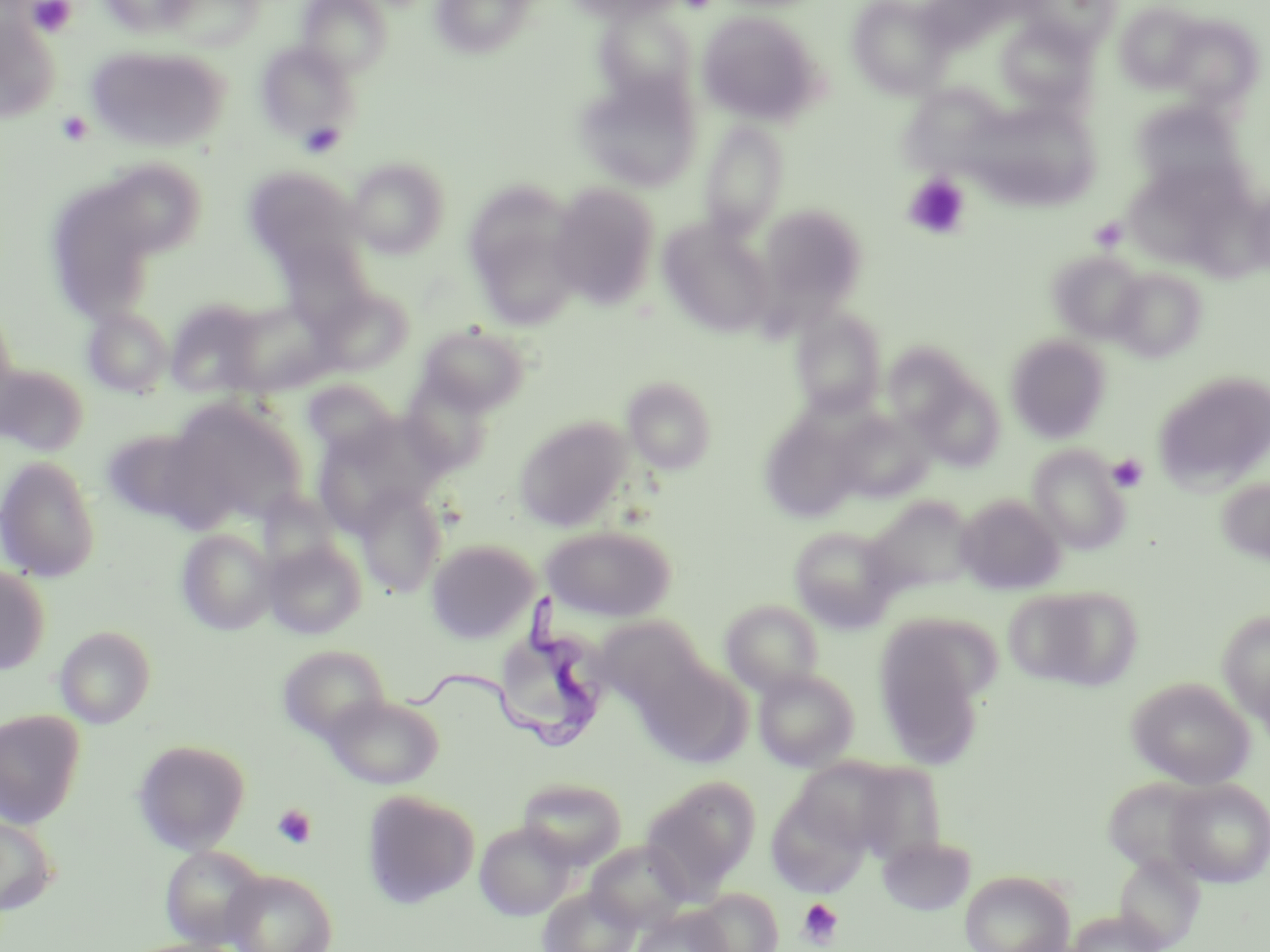
{
  "slide_level_diagnosis": "Trypanosoma brucei",
  "platelet_locations": "approximate bounding boxes as (x1,y1)-(x2,y2) corner pairs in pixels: (26,0)-(78,38), (56,110)-(93,147), (903,174)-(971,240), (1089,217)-(1128,251), (1107,453)-(1148,493), (272,804)-(316,849), (799,898)-(843,948)",
  "field_of_view": "single",
  "image_size": "1270×952 pixels",
  "preparation": "thin blood film",
  "uninfected_red_blood_cell_locations": "approximate bounding boxes as (x1,y1)-(x2,y2) corner pairs in pixels: (99,0)-(199,39), (298,0)-(392,78), (565,0)-(685,22), (847,0)-(955,99), (161,1)-(266,52), (431,1)-(535,58), (1022,1)-(1122,52), (1114,3)-(1205,92), (593,7)-(698,106), (698,11)-(822,124), (0,12)-(60,124), (1164,15)-(1264,108), (997,19)-(1097,111), (255,41)-(359,143), (86,44)-(229,152), (576,72)-(703,192), (901,80)-(1004,189), (1130,100)-(1244,196), (984,106)-(1099,217), (296,118)-(351,159), (699,121)-(790,238), (347,157)-(451,259), (242,165)-(363,274), (108,166)-(208,263), (548,182)-(661,308), (466,186)-(584,328), (48,187)-(148,316), (756,203)-(867,317), (1089,216)-(1128,252), (658,218)-(776,338), (274,239)-(375,332), (1048,250)-(1149,344), (1108,267)-(1207,363), (316,287)-(414,376), (165,298)-(264,398), (228,304)-(335,396), (83,307)-(173,398), (792,307)-(887,418), (0,309)-(20,420), (416,321)-(532,416), (1006,334)-(1111,442), (885,343)-(978,435), (0,363)-(88,457), (1153,371)-(1270,492), (913,373)-(1005,471), (400,374)-(495,475), (622,375)-(718,475), (302,379)-(397,461), (161,398)-(308,528), (759,412)-(864,524), (833,413)-(932,503), (313,415)-(446,532), (514,416)-(632,532), (99,426)-(211,528), (1028,444)-(1131,555), (0,454)-(101,583), (1216,476)-(1270,566), (354,486)-(448,597), (956,493)-(1065,594), (863,495)-(977,598), (541,525)-(677,622), (789,525)-(899,630), (176,529)-(276,635), (263,539)-(367,639), (426,539)-(539,643), (0,564)-(51,675), (1005,585)-(1143,692), (720,600)-(824,696), (898,608)-(1001,717), (1216,609)-(1270,723), (592,615)-(709,713), (55,625)-(156,728), (872,631)-(979,754), (277,645)-(390,743), (638,655)-(751,767), (753,668)-(859,771), (1127,676)-(1255,789), (323,694)-(444,788), (0,708)-(85,828), (132,739)-(252,853), (791,755)-(917,858), (641,775)-(760,897), (1102,776)-(1211,875), (517,778)-(627,867), (1164,778)-(1270,887), (362,789)-(480,909), (767,793)-(869,898), (0,815)-(59,916), (474,821)-(576,920), (877,835)-(976,916), (585,840)-(692,933), (161,846)-(266,948), (1114,853)-(1204,951), (222,869)-(338,952), (960,870)-(1075,952), (539,886)-(641,952), (691,888)-(783,952), (632,907)-(731,952), (1064,911)-(1169,952)",
  "trypanosoma_brucei_locations": "approximate bounding boxes as (x1,y1)-(x2,y2) corner pairs in pixels: (400,587)-(600,749)",
  "magnification": "1000x",
  "modality": "light microscopy",
  "stain": "May-Grünwald-Giemsa"
}